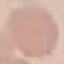 Result: no malaria parasites detected. Cell patch, automatically extracted from a larger field of view and resized to 64 × 64 pixels. Thin smear of blood. Giemsa stain. Acquired by smartphone through the microscope eyepiece.